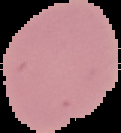
Summary:
  - Image type: segmented cell region with the area outside set to black
  - Result: negative for Plasmodium parasites
  - Preparation: thin blood film
  - Image size: 121×133 pixels